Classify this cell by malaria status.
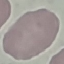

It is uninfected.

Giemsa-stained preparation. Acquired by smartphone through the microscope eyepiece. Thin blood smear. Cell patch, automatically extracted from a larger field of view and resized to 64 × 64 pixels.